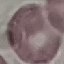

result = no malaria parasites seen
image type = automatically extracted cell patch, resized to 64 × 64 pixels
capture = smartphone through the microscope eyepiece
stain = Giemsa
preparation = thin blood film